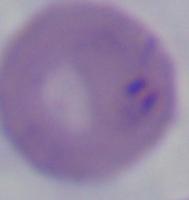

Captured at 1000x magnification. Micrograph. A Babesia parasite is shown.